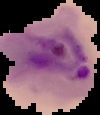

Summary:
  - Image type: segmented cell region on a black background
  - Malaria status: parasitized
  - Preparation: thin blood smear
  - Image size: 100×115 pixels